Comment on the morphology of the erythrocytes.
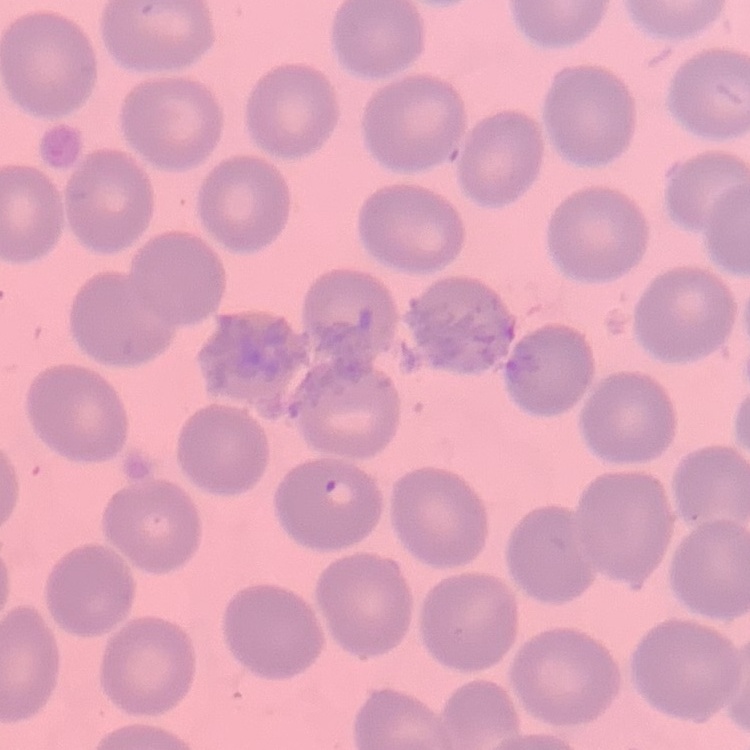
They show no rouleaux formation.

Thin blood film. Stained with either Field's or Giemsa. Square crop of a larger photomicrograph.